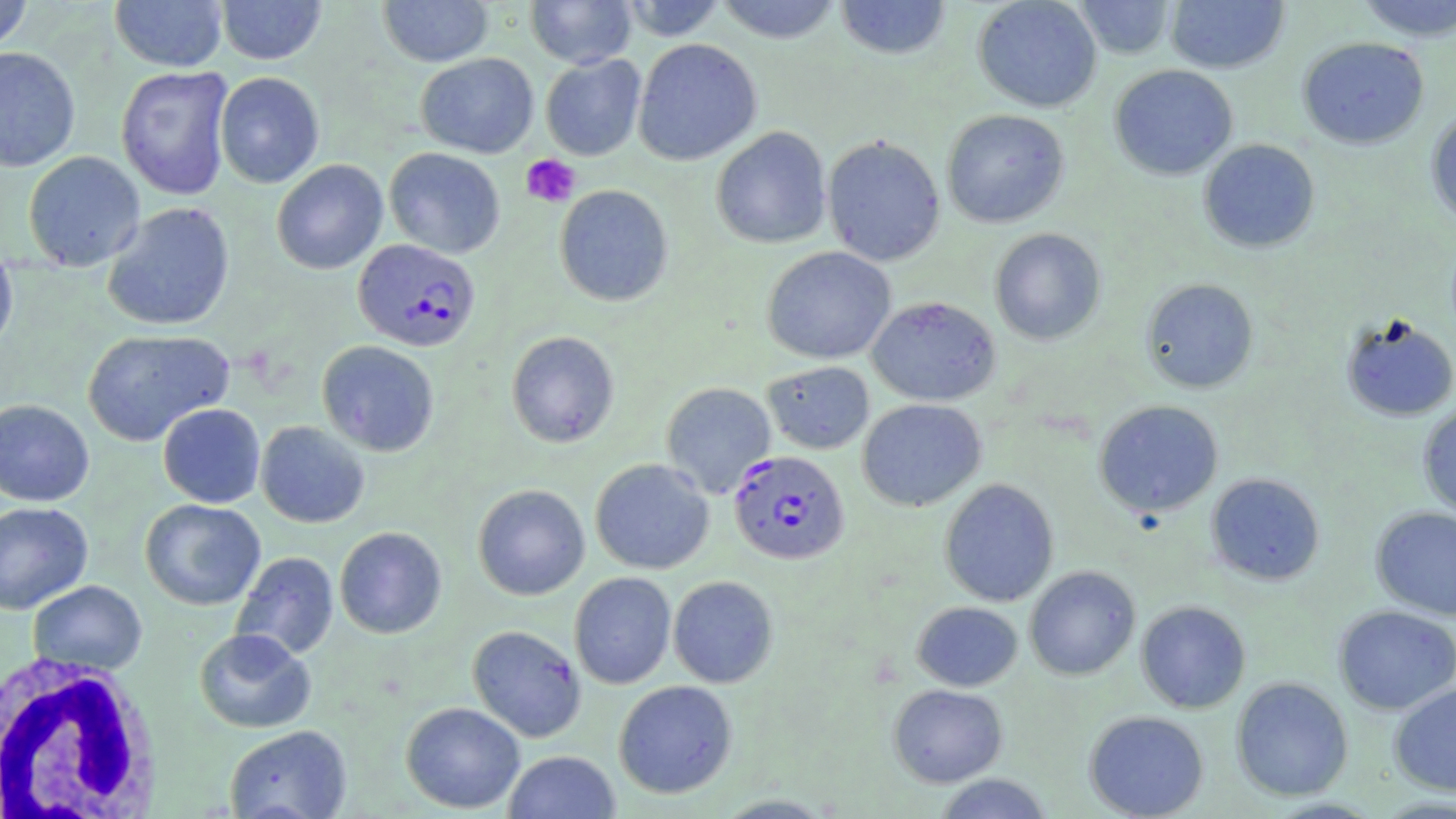
{
  "slide_level_diagnosis": "Plasmodium falciparum",
  "preparation": "thin blood smear",
  "plasmodium_falciparum_infected_red_blood_cell_locations": "approximate bounding boxes as (x1,y1)-(x2,y2) corner pairs in pixels: (352,238)-(481,352), (728,450)-(850,565)",
  "field_of_view": "single",
  "image_size": "1456×819 pixels",
  "uninfected_red_blood_cell_locations": "approximate bounding boxes as (x1,y1)-(x2,y2) corner pairs in pixels: (110,0)-(228,72), (215,0)-(327,65), (377,0)-(493,67), (525,0)-(637,68), (618,0)-(727,41), (714,0)-(844,43), (834,0)-(952,60), (973,0)-(1102,113), (1073,0)-(1176,59), (1354,0)-(1456,42), (0,1)-(34,56), (1165,1)-(1289,73), (1297,36)-(1429,149), (633,38)-(762,166), (0,46)-(81,172), (416,53)-(539,158), (540,54)-(646,161), (1109,64)-(1238,181), (115,67)-(233,200), (215,71)-(324,188), (941,108)-(1070,229), (1425,108)-(1456,229), (711,126)-(831,249), (822,135)-(946,267), (1198,139)-(1320,253), (384,147)-(505,259), (22,151)-(145,272), (271,158)-(388,275), (554,184)-(673,307), (102,201)-(235,332), (989,228)-(1106,345), (0,240)-(18,359), (761,246)-(896,365), (1140,278)-(1259,394), (867,296)-(1001,406), (1339,314)-(1456,422), (82,328)-(234,446), (506,330)-(619,448), (317,340)-(439,456), (763,361)-(874,455), (660,381)-(776,499), (857,398)-(987,511), (0,399)-(94,507), (1093,400)-(1224,518), (1417,402)-(1456,521), (157,403)-(265,508), (255,421)-(370,528), (589,458)-(715,574), (1205,472)-(1326,586), (939,478)-(1059,607), (473,484)-(590,600), (140,498)-(266,610), (0,501)-(93,614), (1370,506)-(1456,621), (334,526)-(447,639), (231,551)-(339,660), (1024,565)-(1141,680), (569,572)-(676,689), (667,575)-(779,688), (27,579)-(147,676), (1135,600)-(1251,714), (912,601)-(1023,691), (1333,604)-(1456,716), (467,624)-(587,742), (194,628)-(316,733), (1230,677)-(1353,801), (613,680)-(738,799), (1388,681)-(1456,796), (888,684)-(1008,788), (400,701)-(525,813), (1083,710)-(1209,819), (224,724)-(352,819), (503,750)-(621,819), (933,773)-(1054,818), (711,793)-(839,818), (1372,796)-(1456,817)",
  "platelet_locations": "approximate bounding boxes as (x1,y1)-(x2,y2) corner pairs in pixels: (521,154)-(580,207)",
  "magnification": "1000x",
  "modality": "light microscopy",
  "white_blood_cell_locations": "approximate bounding boxes as (x1,y1)-(x2,y2) corner pairs in pixels: (0,654)-(163,819)",
  "stain": "May-Grünwald-Giemsa"
}